Classify this cell by malaria status.
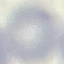

It is uninfected.

Summary:
  - Preparation: thin smear
  - Stain: Giemsa
  - Capture: smartphone through the microscope eyepiece
  - Image type: automatically extracted cell patch, resized to 64 × 64 pixels